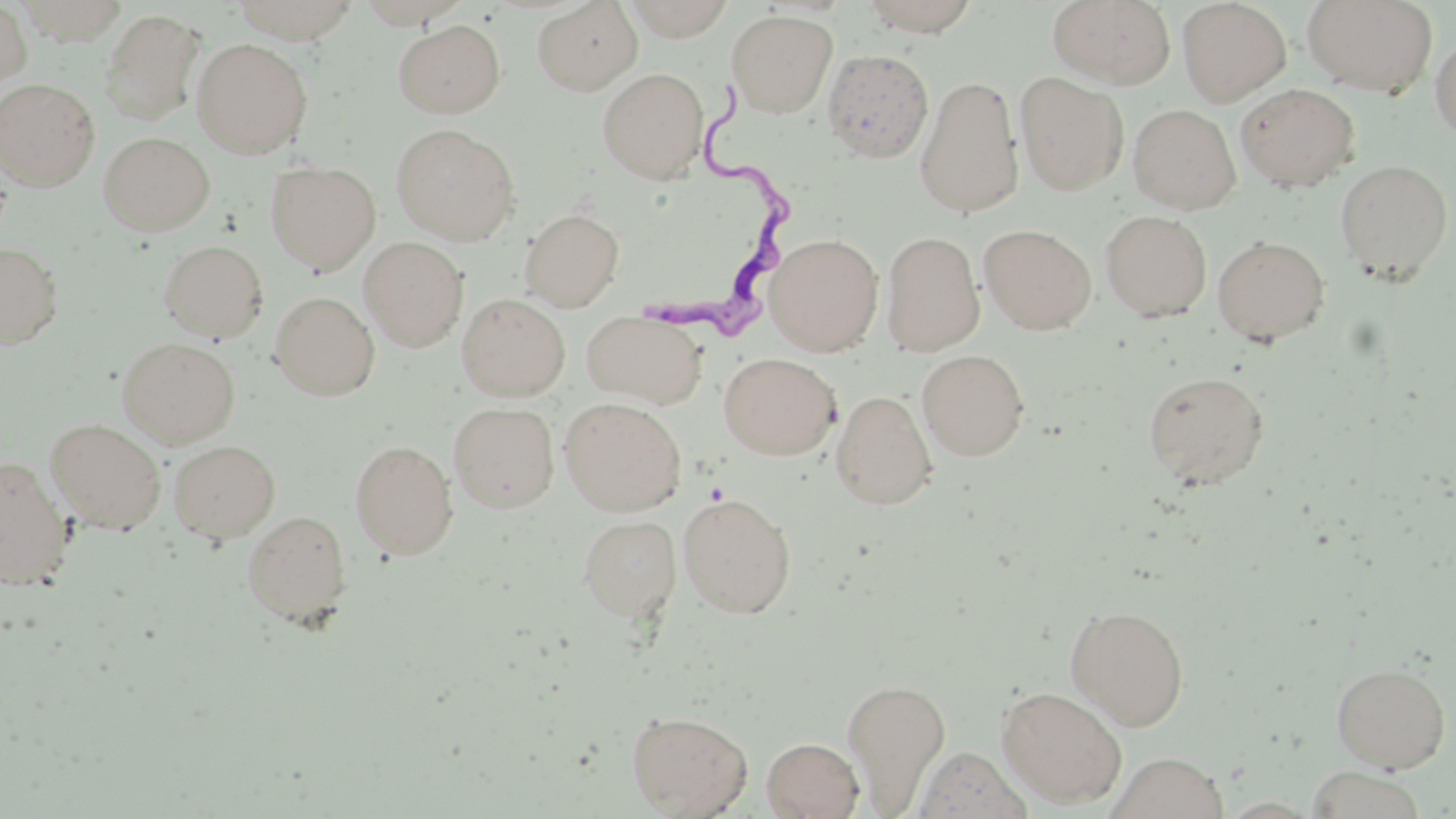
slide-level diagnosis = Trypanosoma brucei
image size = 1456×819 pixels
modality = light microscopy
field of view = single
preparation = thin blood smear
uninfected red blood cell locations = approximate bounding boxes as named x1/y1/x2/y2 corners in pixels: (x1=12, y1=0, x2=129, y2=44), (x1=231, y1=0, x2=363, y2=43), (x1=619, y1=0, x2=739, y2=41), (x1=859, y1=0, x2=983, y2=36), (x1=1047, y1=0, x2=1176, y2=88), (x1=1302, y1=0, x2=1438, y2=96), (x1=0, y1=1, x2=32, y2=89), (x1=532, y1=1, x2=643, y2=95), (x1=1177, y1=1, x2=1291, y2=106), (x1=99, y1=8, x2=205, y2=126), (x1=726, y1=10, x2=837, y2=117), (x1=393, y1=19, x2=505, y2=118), (x1=1430, y1=32, x2=1456, y2=143), (x1=192, y1=38, x2=312, y2=158), (x1=822, y1=49, x2=934, y2=163), (x1=598, y1=68, x2=708, y2=183), (x1=1015, y1=72, x2=1128, y2=196), (x1=915, y1=76, x2=1024, y2=218), (x1=0, y1=78, x2=100, y2=190), (x1=1236, y1=83, x2=1359, y2=192), (x1=1128, y1=104, x2=1240, y2=214), (x1=391, y1=124, x2=520, y2=245), (x1=99, y1=132, x2=214, y2=234), (x1=1335, y1=160, x2=1453, y2=283), (x1=266, y1=161, x2=380, y2=275), (x1=519, y1=208, x2=624, y2=311), (x1=1100, y1=210, x2=1212, y2=321), (x1=979, y1=224, x2=1096, y2=334), (x1=881, y1=231, x2=984, y2=355), (x1=766, y1=233, x2=883, y2=356), (x1=1212, y1=234, x2=1329, y2=346), (x1=359, y1=236, x2=469, y2=352), (x1=158, y1=239, x2=268, y2=342), (x1=0, y1=242, x2=63, y2=349), (x1=270, y1=292, x2=380, y2=400), (x1=457, y1=293, x2=570, y2=401), (x1=582, y1=311, x2=706, y2=408), (x1=118, y1=337, x2=240, y2=448), (x1=917, y1=349, x2=1030, y2=460), (x1=719, y1=353, x2=840, y2=460), (x1=1143, y1=370, x2=1270, y2=489), (x1=831, y1=391, x2=937, y2=509), (x1=559, y1=397, x2=686, y2=516), (x1=449, y1=402, x2=560, y2=513), (x1=46, y1=419, x2=166, y2=533), (x1=168, y1=439, x2=280, y2=543), (x1=350, y1=440, x2=458, y2=560), (x1=0, y1=456, x2=73, y2=589), (x1=678, y1=492, x2=797, y2=618), (x1=242, y1=510, x2=352, y2=625), (x1=578, y1=515, x2=681, y2=621), (x1=1065, y1=604, x2=1190, y2=730), (x1=1330, y1=662, x2=1451, y2=772), (x1=842, y1=677, x2=951, y2=811), (x1=996, y1=686, x2=1127, y2=808), (x1=627, y1=710, x2=752, y2=817), (x1=762, y1=737, x2=864, y2=819), (x1=1107, y1=752, x2=1228, y2=819), (x1=1304, y1=766, x2=1428, y2=819)
magnification = 1000x
Trypanosoma brucei locations = approximate bounding boxes as named x1/y1/x2/y2 corners in pixels: (x1=639, y1=82, x2=796, y2=348)
stain = May-Grünwald-Giemsa